Give the extent of all Plasmodium vivax-infected red blood cells.
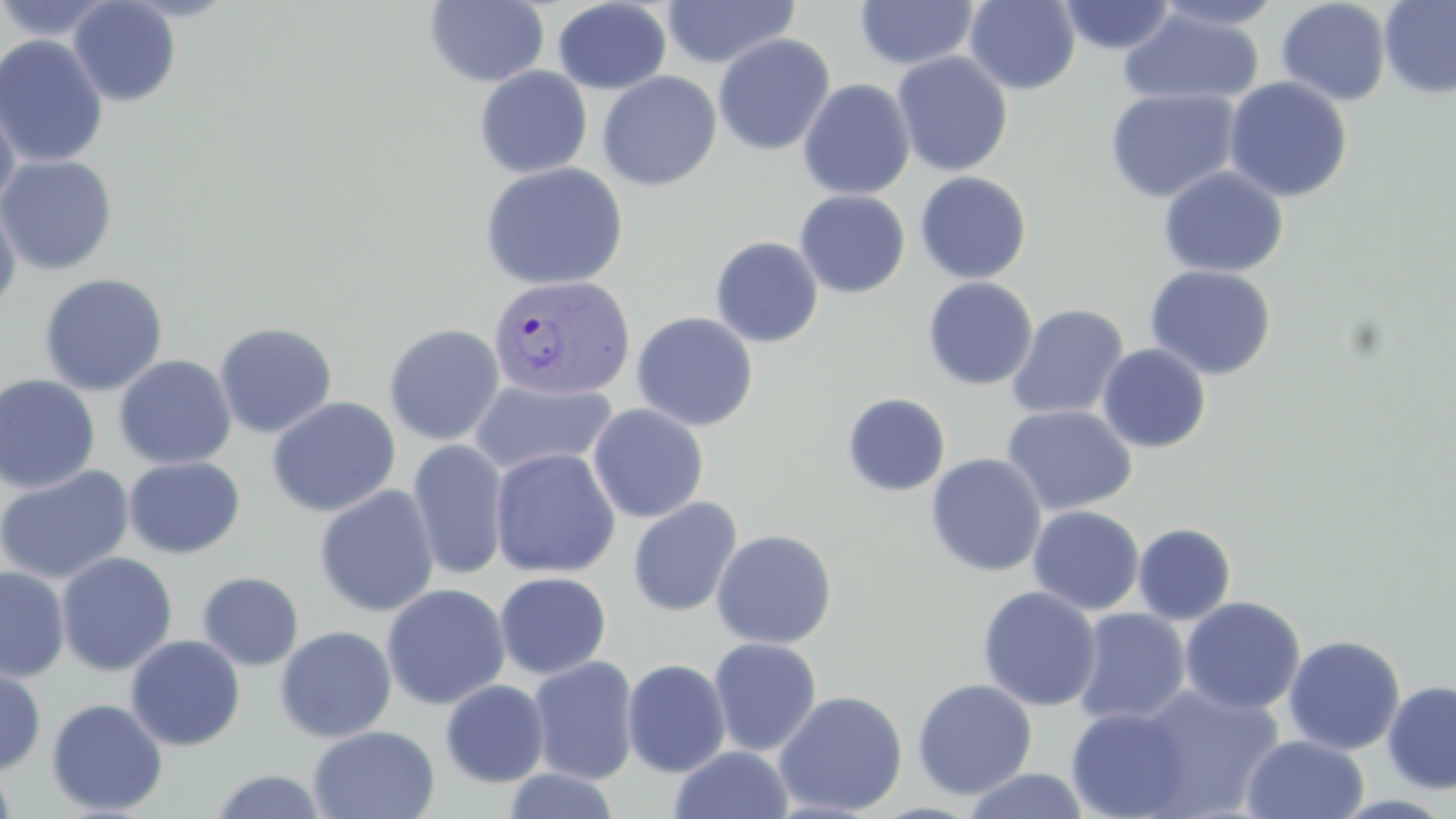
Approximate bounding boxes as named x1/y1/x2/y2 corners in pixels.
Plasmodium vivax-infected red blood cells: (x1=487, y1=274, x2=636, y2=400).

Uninfected red blood cell locations: (x1=0, y1=0, x2=117, y2=42), (x1=67, y1=0, x2=181, y2=107), (x1=424, y1=0, x2=549, y2=88), (x1=964, y1=0, x2=1081, y2=94), (x1=1152, y1=0, x2=1286, y2=30), (x1=1379, y1=0, x2=1456, y2=99), (x1=552, y1=1, x2=671, y2=94), (x1=662, y1=1, x2=801, y2=69), (x1=855, y1=1, x2=979, y2=70), (x1=1058, y1=1, x2=1177, y2=55), (x1=1276, y1=1, x2=1391, y2=106), (x1=1118, y1=8, x2=1265, y2=108), (x1=713, y1=33, x2=835, y2=156), (x1=0, y1=35, x2=109, y2=168), (x1=892, y1=51, x2=1014, y2=177), (x1=474, y1=66, x2=593, y2=179), (x1=597, y1=71, x2=722, y2=191), (x1=1223, y1=76, x2=1353, y2=202), (x1=797, y1=78, x2=916, y2=200), (x1=1104, y1=87, x2=1242, y2=203), (x1=0, y1=93, x2=21, y2=214), (x1=0, y1=155, x2=117, y2=275), (x1=478, y1=162, x2=629, y2=291), (x1=1158, y1=166, x2=1289, y2=279), (x1=914, y1=171, x2=1032, y2=284), (x1=793, y1=189, x2=911, y2=298), (x1=0, y1=198, x2=21, y2=313), (x1=710, y1=236, x2=824, y2=348), (x1=1145, y1=264, x2=1277, y2=381), (x1=38, y1=273, x2=169, y2=396), (x1=922, y1=277, x2=1038, y2=391), (x1=1006, y1=304, x2=1129, y2=420), (x1=631, y1=311, x2=759, y2=431), (x1=213, y1=321, x2=338, y2=438), (x1=383, y1=323, x2=505, y2=446), (x1=1096, y1=343, x2=1211, y2=453), (x1=113, y1=354, x2=237, y2=470), (x1=0, y1=373, x2=100, y2=493), (x1=469, y1=379, x2=616, y2=477), (x1=841, y1=392, x2=951, y2=497), (x1=266, y1=396, x2=401, y2=517), (x1=587, y1=404, x2=709, y2=523), (x1=1001, y1=404, x2=1138, y2=516), (x1=408, y1=438, x2=510, y2=580), (x1=490, y1=447, x2=620, y2=578), (x1=925, y1=452, x2=1048, y2=577), (x1=124, y1=456, x2=245, y2=558), (x1=0, y1=465, x2=135, y2=585), (x1=314, y1=485, x2=440, y2=617), (x1=627, y1=497, x2=743, y2=617), (x1=1027, y1=505, x2=1145, y2=615), (x1=1132, y1=523, x2=1237, y2=625), (x1=711, y1=529, x2=837, y2=649), (x1=56, y1=551, x2=178, y2=676), (x1=0, y1=565, x2=70, y2=682), (x1=197, y1=571, x2=304, y2=671), (x1=494, y1=572, x2=612, y2=679), (x1=381, y1=583, x2=511, y2=710), (x1=977, y1=586, x2=1102, y2=711), (x1=1179, y1=596, x2=1305, y2=715), (x1=1073, y1=607, x2=1191, y2=726), (x1=274, y1=625, x2=397, y2=743), (x1=125, y1=634, x2=246, y2=751), (x1=1283, y1=634, x2=1406, y2=755), (x1=708, y1=637, x2=822, y2=756), (x1=528, y1=655, x2=639, y2=785), (x1=622, y1=658, x2=731, y2=777), (x1=0, y1=661, x2=47, y2=777), (x1=912, y1=678, x2=1037, y2=799), (x1=440, y1=679, x2=550, y2=787), (x1=1382, y1=679, x2=1456, y2=795), (x1=1132, y1=683, x2=1285, y2=818), (x1=773, y1=690, x2=908, y2=815), (x1=46, y1=698, x2=168, y2=816), (x1=1066, y1=706, x2=1192, y2=819), (x1=308, y1=725, x2=440, y2=819), (x1=1240, y1=734, x2=1370, y2=819), (x1=669, y1=745, x2=794, y2=819), (x1=0, y1=761, x2=17, y2=819), (x1=502, y1=767, x2=621, y2=818), (x1=207, y1=768, x2=331, y2=819), (x1=961, y1=768, x2=1092, y2=819). Slide-level diagnosis: Plasmodium vivax. May-Grünwald-Giemsa-stained preparation. Thin blood film. Image is 1456×819 pixels. Optical microscopy. One field of a larger specimen. 1000x magnification.